Comment on the morphology of the red blood cells.
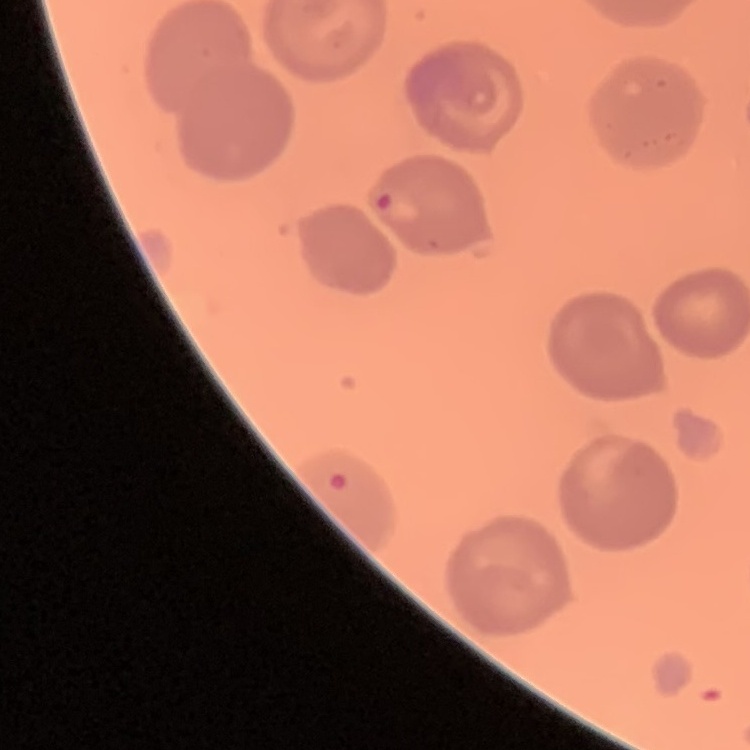
No rouleaux formation.

Summary:
  - Image type: one tile cut from a larger photomicrograph
  - Preparation: thin peripheral smear
  - Stain: Field's or Giemsa